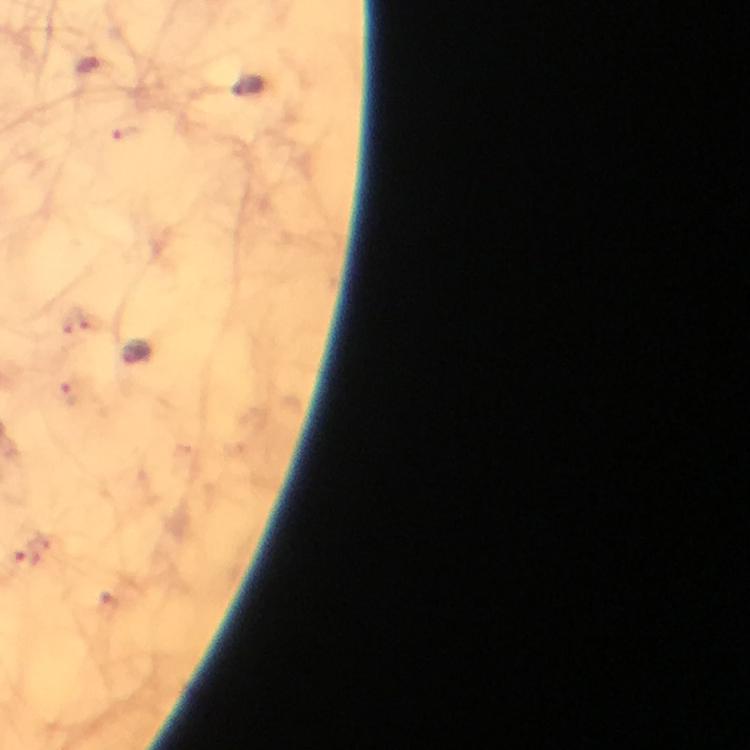

immersion oil = applied
image size = 750×750 pixels
cropped from = a single field of view
context = from a diagnostic examination for malaria
preparation = thick blood smear
capture = smartphone photograph through a microscope
stain = Giemsa
Plasmodium parasite locations = approximate object centers, in pixels from the top-left corner: (x=87, y=65), (x=26, y=557)
magnification = 100x